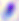
modality: photomicrograph
magnification: 400x
identification: Toxoplasma gondii